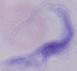

modality = photomicrograph
identification = trypanosome
magnification = 1000x